Identify the parasite.
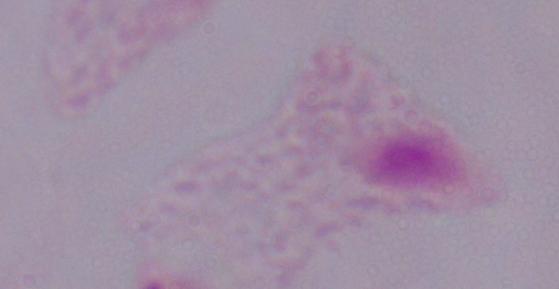
This is a trichomonad.

Micrograph. 1000x magnification.